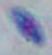
Summary:
  - Modality: photomicrograph
  - Identification: Toxoplasma gondii
  - Magnification: 1000x